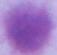
Summary:
  - Magnification: 1000x
  - Modality: photomicrograph
  - Identification: erythrocyte